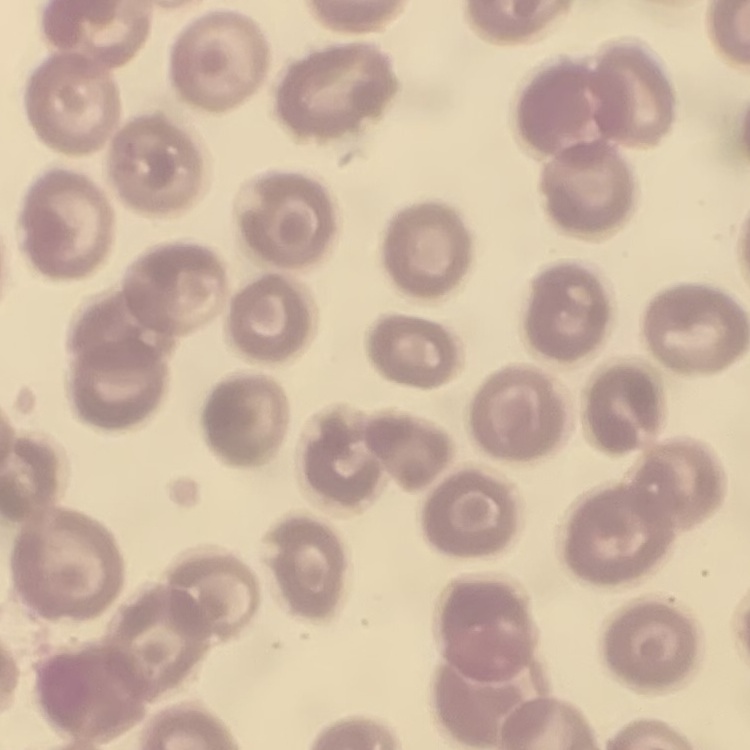 The erythrocytes exhibit no rouleaux formation. Thin peripheral smear. Stained with either Field's or Giemsa. One tile cut from a larger photomicrograph.